Locate every Plasmodium parasite.
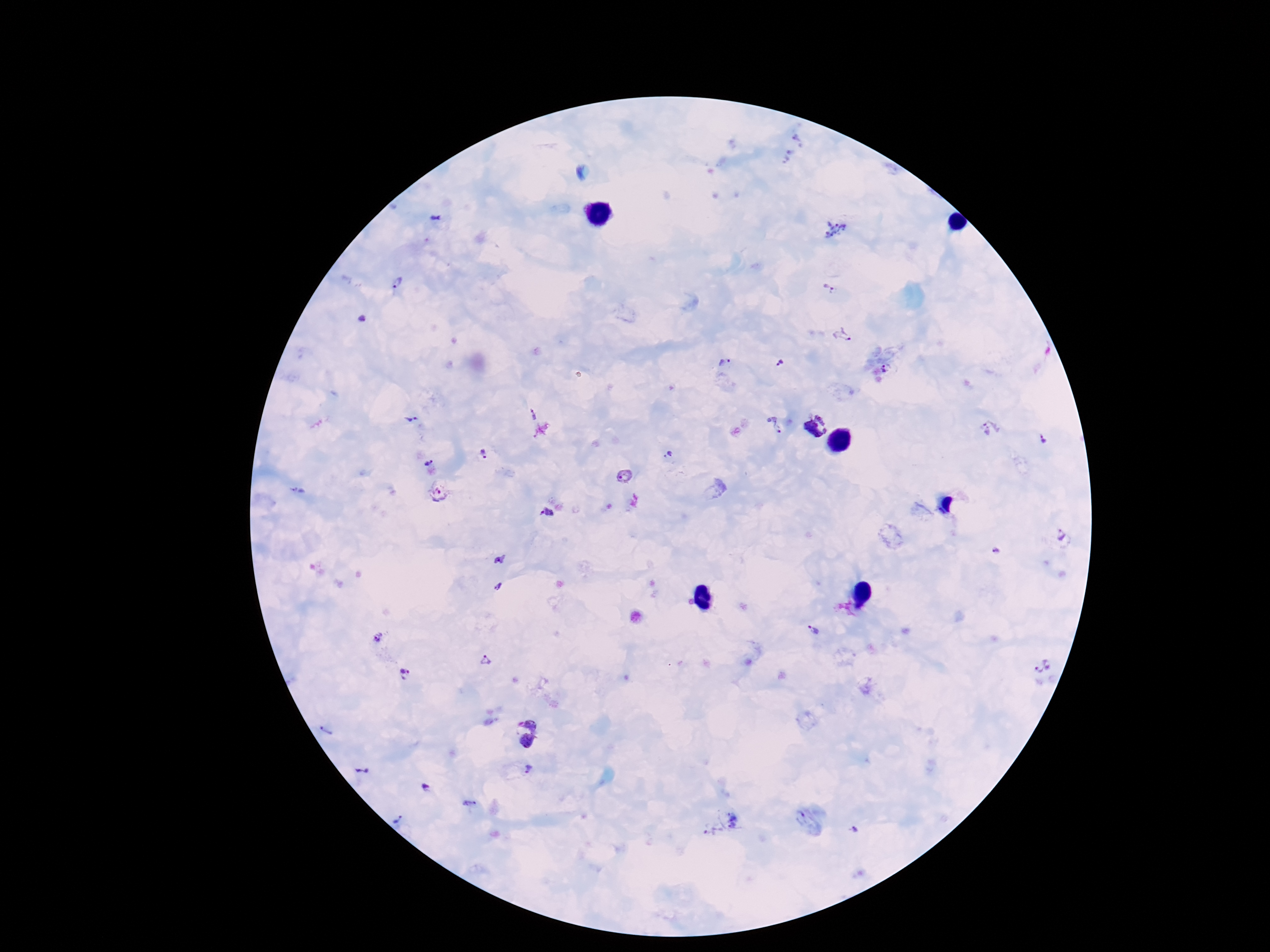
Approximate object centers, in pixels from the top-left corner.
Plasmodium parasites: (x=792, y=150), (x=434, y=217), (x=837, y=230), (x=401, y=284), (x=829, y=289), (x=362, y=318), (x=842, y=335), (x=725, y=363), (x=779, y=364), (x=888, y=368), (x=533, y=414), (x=413, y=421), (x=774, y=425), (x=817, y=426), (x=991, y=429), (x=1042, y=438), (x=670, y=454), (x=484, y=455), (x=431, y=464), (x=626, y=477), (x=439, y=495), (x=545, y=514), (x=1059, y=533), (x=996, y=553), (x=500, y=560), (x=499, y=586), (x=812, y=631), (x=377, y=637), (x=485, y=660), (x=1050, y=661), (x=404, y=672), (x=1039, y=672), (x=525, y=730), (x=328, y=731), (x=528, y=769), (x=363, y=773), (x=426, y=788), (x=470, y=802), (x=397, y=819), (x=854, y=829), (x=721, y=835).

patient malaria status = infected
magnification = 100x
preparation = thick peripheral-blood smear
capture = smartphone camera through the microscope eyepiece
stain = Giemsa
image size = 1270×952 pixels
field of view = single